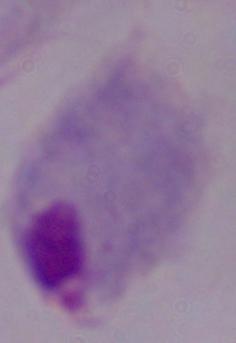
Summary:
  - Modality: photomicrograph
  - Magnification: 1000x
  - Identification: trichomonad